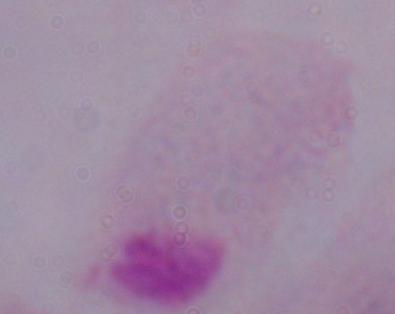

Captured at 1000x magnification. Photomicrograph. A trichomonad is shown.